Locate every blood parasite and identify its species.
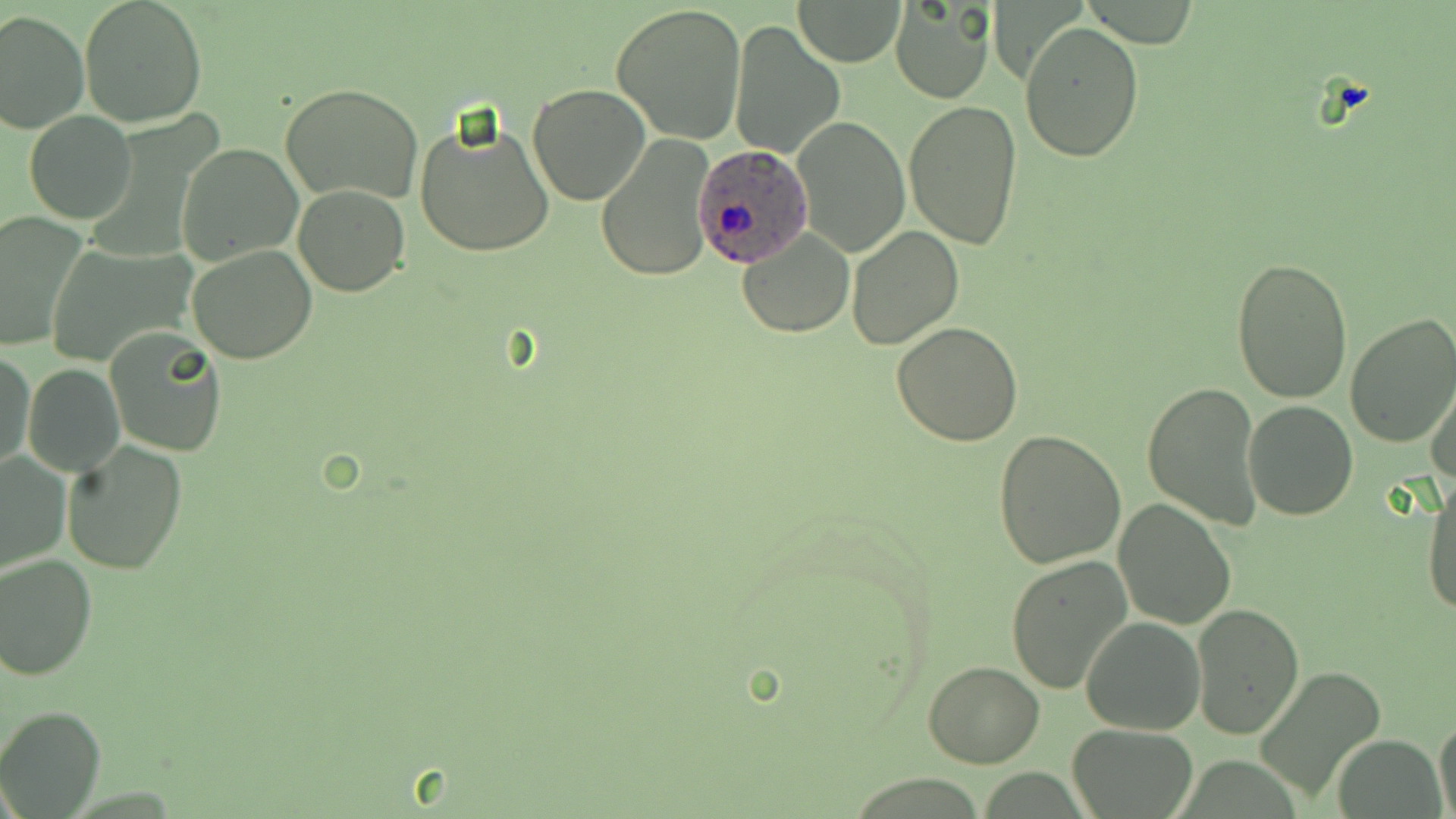

Approximate bounding boxes as named x1/y1/x2/y2 corners in pixels.
Plasmodium ovale-infected red blood cells: (x1=692, y1=149, x2=812, y2=264).
No Plasmodium falciparum, Plasmodium malariae, Plasmodium vivax, Babesia divergens, or Trypanosoma brucei observed.

Uninfected red blood cell locations: (x1=78, y1=0, x2=208, y2=128), (x1=793, y1=0, x2=907, y2=66), (x1=889, y1=1, x2=996, y2=105), (x1=612, y1=2, x2=747, y2=144), (x1=0, y1=10, x2=88, y2=133), (x1=730, y1=20, x2=846, y2=158), (x1=1021, y1=22, x2=1144, y2=163), (x1=281, y1=82, x2=423, y2=205), (x1=528, y1=83, x2=649, y2=205), (x1=904, y1=100, x2=1023, y2=249), (x1=24, y1=109, x2=137, y2=225), (x1=410, y1=115, x2=558, y2=258), (x1=791, y1=115, x2=909, y2=257), (x1=595, y1=134, x2=716, y2=283), (x1=176, y1=143, x2=300, y2=265), (x1=293, y1=184, x2=409, y2=296), (x1=0, y1=211, x2=88, y2=353), (x1=846, y1=225, x2=964, y2=349), (x1=736, y1=228, x2=854, y2=337), (x1=43, y1=243, x2=196, y2=369), (x1=187, y1=245, x2=317, y2=365), (x1=1230, y1=256, x2=1354, y2=404), (x1=1344, y1=313, x2=1456, y2=449), (x1=891, y1=323, x2=1023, y2=445), (x1=104, y1=328, x2=228, y2=456), (x1=1, y1=351, x2=35, y2=475), (x1=24, y1=363, x2=125, y2=477), (x1=1427, y1=366, x2=1456, y2=490), (x1=1142, y1=380, x2=1264, y2=529), (x1=1242, y1=399, x2=1359, y2=520), (x1=992, y1=429, x2=1127, y2=569), (x1=62, y1=440, x2=187, y2=574), (x1=0, y1=450, x2=71, y2=574), (x1=1421, y1=476, x2=1455, y2=621), (x1=1113, y1=498, x2=1237, y2=628), (x1=1, y1=553, x2=99, y2=681), (x1=1005, y1=554, x2=1132, y2=695), (x1=1190, y1=604, x2=1304, y2=737), (x1=1080, y1=615, x2=1205, y2=735), (x1=922, y1=661, x2=1045, y2=768), (x1=1258, y1=666, x2=1387, y2=802), (x1=0, y1=705, x2=105, y2=816), (x1=1433, y1=717, x2=1456, y2=819), (x1=1068, y1=723, x2=1199, y2=817), (x1=1334, y1=733, x2=1444, y2=819). Slide-level diagnosis: Plasmodium ovale. Image is 1456×819 pixels. 1000x magnification. Single field of view. May-Grünwald-Giemsa stain. Optical microscopy. Thin blood film.